Give the preparation type.
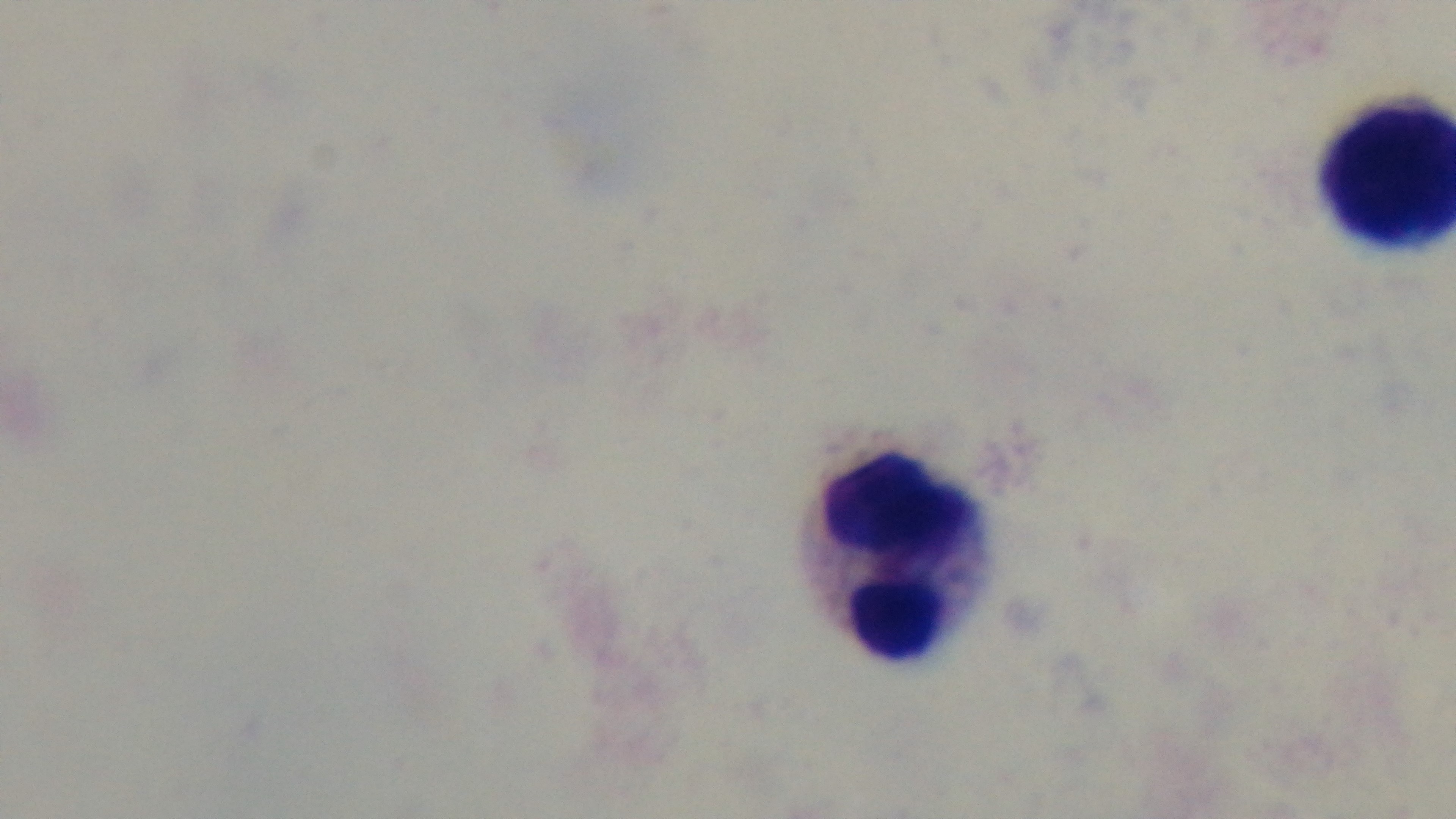

A thick smear.

{
  "field_of_view": "one from the slide",
  "modality": "light microscopy",
  "stain": "Giemsa",
  "malaria_status": "negative",
  "capture": "mounted 4K digital camera",
  "objective": "100x oil immersion"
}